Assess the morphology of the erythrocytes.
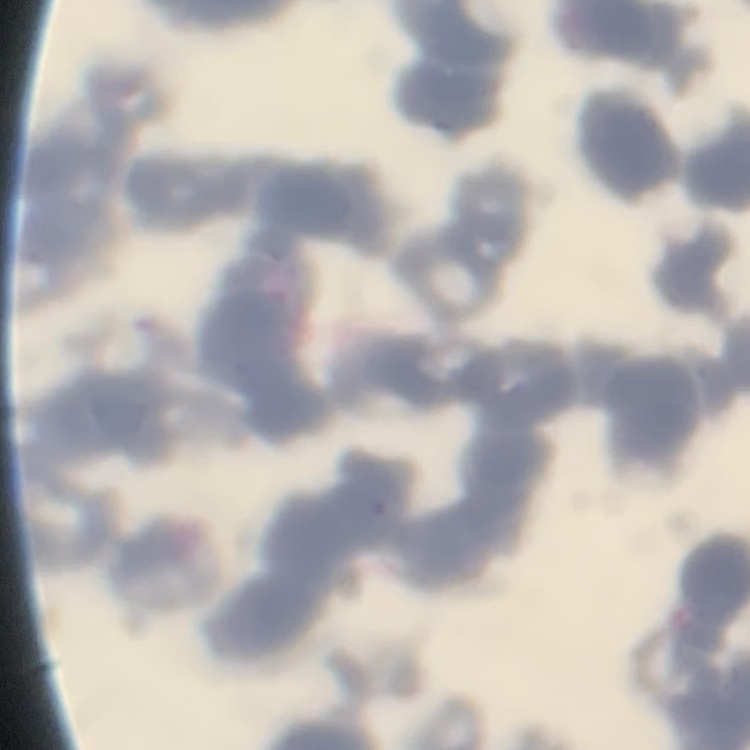

Rouleaux formation.

{
  "image_type": "square crop of a larger photomicrograph",
  "preparation": "thin blood film",
  "stain": "Field's or Giemsa"
}